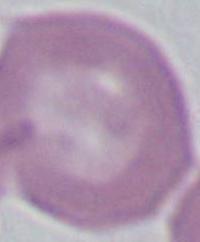

1000x magnification. A red blood cell is seen. Photomicrograph.